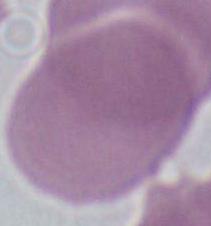

identification = erythrocyte
modality = micrograph
magnification = 1000x